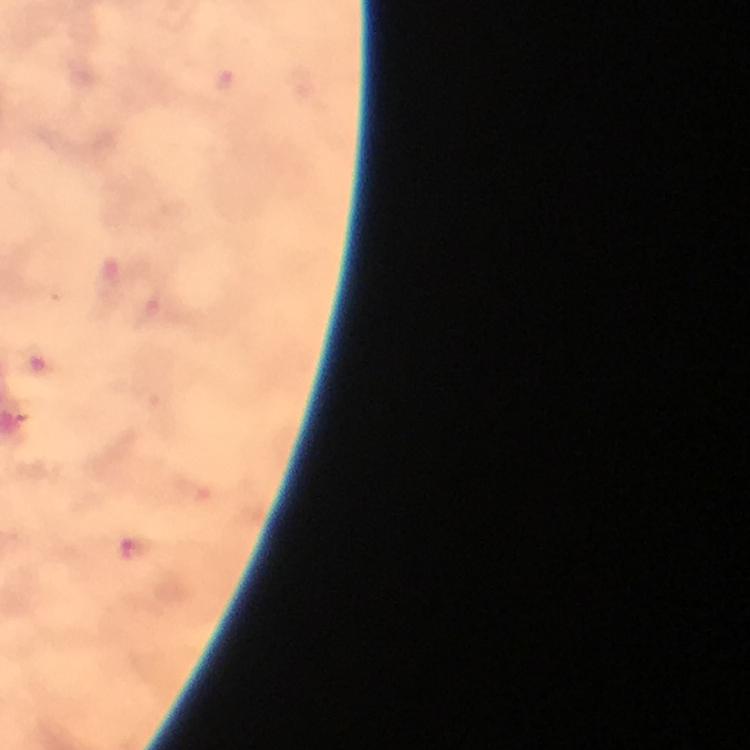

image size = 750×750 pixels
context = from a malaria diagnostic workup
Plasmodium parasite locations = approximate centers as (x, y) in pixels: (225, 84), (134, 550)
stain = Giemsa
preparation = thick smear
capture = smartphone mounted on the microscope
magnification = 100x
immersion oil = used
cropped from = one field of view